Name the cell type shown.
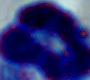

This is a leukocyte.

1000x magnification. Micrograph.